Identify the blood parasite species.
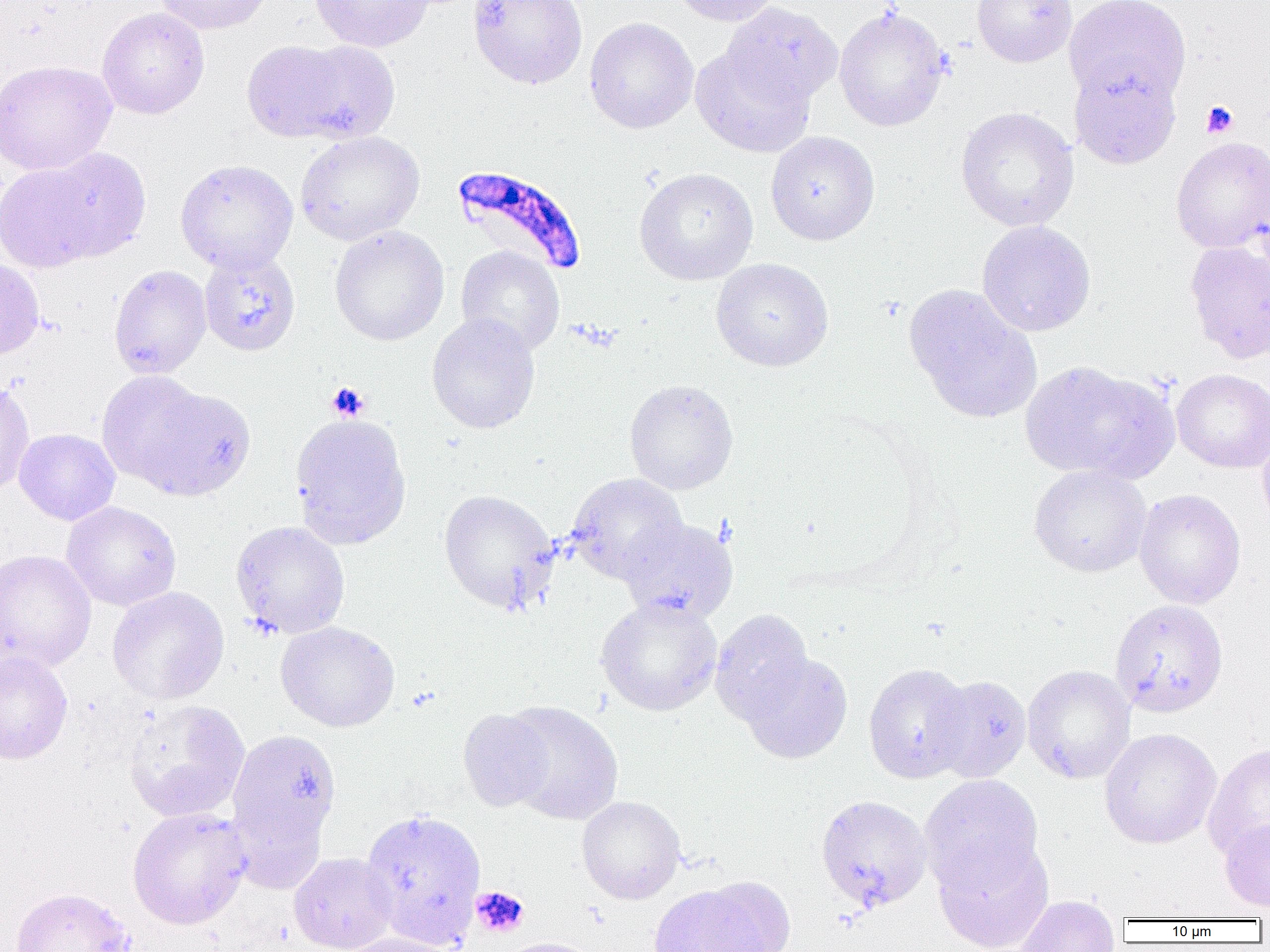

Plasmodium falciparum.

Summary:
  - Coordinate format: approximate bounding boxes as named x1/y1/x2/y2 corners in pixels
  - Uninfected red blood cell locations: (x1=153, y1=0, x2=276, y2=35), (x1=310, y1=0, x2=433, y2=52), (x1=468, y1=0, x2=588, y2=89), (x1=669, y1=0, x2=781, y2=26), (x1=972, y1=0, x2=1077, y2=67), (x1=1064, y1=0, x2=1192, y2=108), (x1=721, y1=2, x2=843, y2=109), (x1=834, y1=5, x2=950, y2=132), (x1=97, y1=7, x2=210, y2=119), (x1=584, y1=17, x2=698, y2=133), (x1=243, y1=39, x2=398, y2=144), (x1=691, y1=45, x2=814, y2=157), (x1=1069, y1=59, x2=1181, y2=169), (x1=0, y1=60, x2=117, y2=175), (x1=955, y1=106, x2=1079, y2=232), (x1=295, y1=131, x2=424, y2=245), (x1=766, y1=131, x2=880, y2=245), (x1=1170, y1=136, x2=1270, y2=253), (x1=42, y1=148, x2=151, y2=260), (x1=175, y1=158, x2=298, y2=274), (x1=0, y1=160, x2=104, y2=273), (x1=634, y1=167, x2=758, y2=285), (x1=976, y1=220, x2=1096, y2=337), (x1=329, y1=225, x2=449, y2=346), (x1=1185, y1=239, x2=1270, y2=364), (x1=456, y1=245, x2=565, y2=356), (x1=198, y1=249, x2=300, y2=356), (x1=0, y1=257, x2=45, y2=360), (x1=711, y1=258, x2=833, y2=372), (x1=108, y1=265, x2=212, y2=379), (x1=904, y1=284, x2=1041, y2=422), (x1=426, y1=313, x2=541, y2=434), (x1=1019, y1=360, x2=1176, y2=482), (x1=1171, y1=368, x2=1270, y2=473), (x1=97, y1=370, x2=210, y2=487), (x1=624, y1=379, x2=739, y2=495), (x1=0, y1=380, x2=35, y2=498), (x1=130, y1=384, x2=255, y2=501), (x1=289, y1=412, x2=411, y2=549), (x1=14, y1=428, x2=120, y2=525), (x1=1257, y1=431, x2=1270, y2=534), (x1=1028, y1=464, x2=1152, y2=577), (x1=566, y1=473, x2=688, y2=584), (x1=438, y1=489, x2=559, y2=614), (x1=1134, y1=489, x2=1246, y2=609), (x1=61, y1=501, x2=182, y2=611), (x1=620, y1=518, x2=738, y2=624), (x1=230, y1=521, x2=350, y2=639), (x1=0, y1=549, x2=96, y2=674), (x1=107, y1=586, x2=229, y2=705), (x1=596, y1=597, x2=723, y2=716), (x1=1109, y1=600, x2=1228, y2=718), (x1=710, y1=609, x2=815, y2=725), (x1=276, y1=621, x2=400, y2=732), (x1=0, y1=650, x2=73, y2=765), (x1=738, y1=651, x2=853, y2=764), (x1=863, y1=663, x2=973, y2=783), (x1=1022, y1=665, x2=1136, y2=784), (x1=927, y1=674, x2=1032, y2=784), (x1=123, y1=699, x2=251, y2=822), (x1=502, y1=701, x2=623, y2=825), (x1=458, y1=708, x2=554, y2=811), (x1=226, y1=728, x2=342, y2=852), (x1=1099, y1=728, x2=1221, y2=849), (x1=1203, y1=743, x2=1270, y2=862), (x1=919, y1=774, x2=1045, y2=894), (x1=815, y1=794, x2=932, y2=913), (x1=576, y1=795, x2=685, y2=904), (x1=227, y1=798, x2=328, y2=895), (x1=127, y1=807, x2=250, y2=929), (x1=360, y1=807, x2=487, y2=949), (x1=1219, y1=818, x2=1270, y2=912), (x1=933, y1=837, x2=1055, y2=952), (x1=289, y1=852, x2=398, y2=952), (x1=648, y1=884, x2=771, y2=952), (x1=11, y1=887, x2=135, y2=952), (x1=1015, y1=894, x2=1120, y2=952), (x1=339, y1=933, x2=459, y2=952), (x1=492, y1=937, x2=604, y2=952)
  - Plasmodium falciparum-infected red blood cell locations: (x1=451, y1=165, x2=587, y2=277)
  - Platelet locations: (x1=1200, y1=100, x2=1238, y2=137), (x1=327, y1=383, x2=369, y2=420), (x1=471, y1=886, x2=529, y2=937)
  - Modality: optical microscopy
  - Preparation: thin blood film
  - Magnification: 1000x
  - Image size: 1270×952 pixels
  - Field of view: single